Assess this cell for malaria.
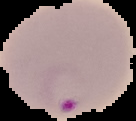
It is parasitized.

{
  "image_size": "136×121 pixels",
  "preparation": "thin blood smear",
  "image_type": "cell region segmented out of the field of view; surrounding area masked to black"
}